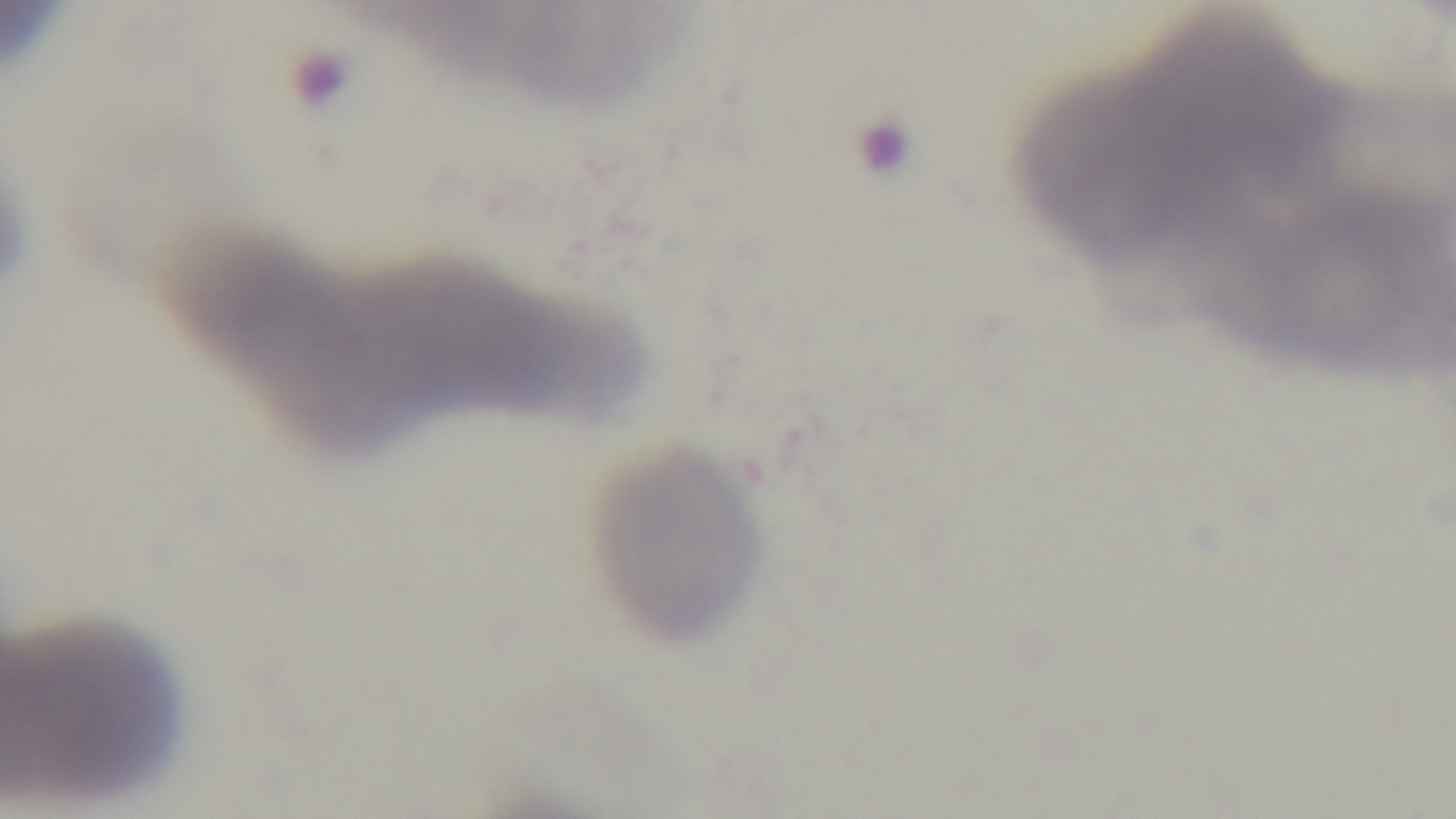

Summary:
  - Field of view: one from the slide
  - Malaria status: negative
  - Objective: 100x oil immersion
  - Modality: light microscopy
  - Capture: mounted 4K digital camera
  - Preparation: thin blood film
  - Stain: Giemsa